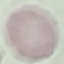
malaria status = uninfected
image type = cell patch, automatically extracted from a larger field of view and resized to 64 × 64 pixels
preparation = thin blood film
capture = smartphone through the microscope eyepiece
stain = Giemsa